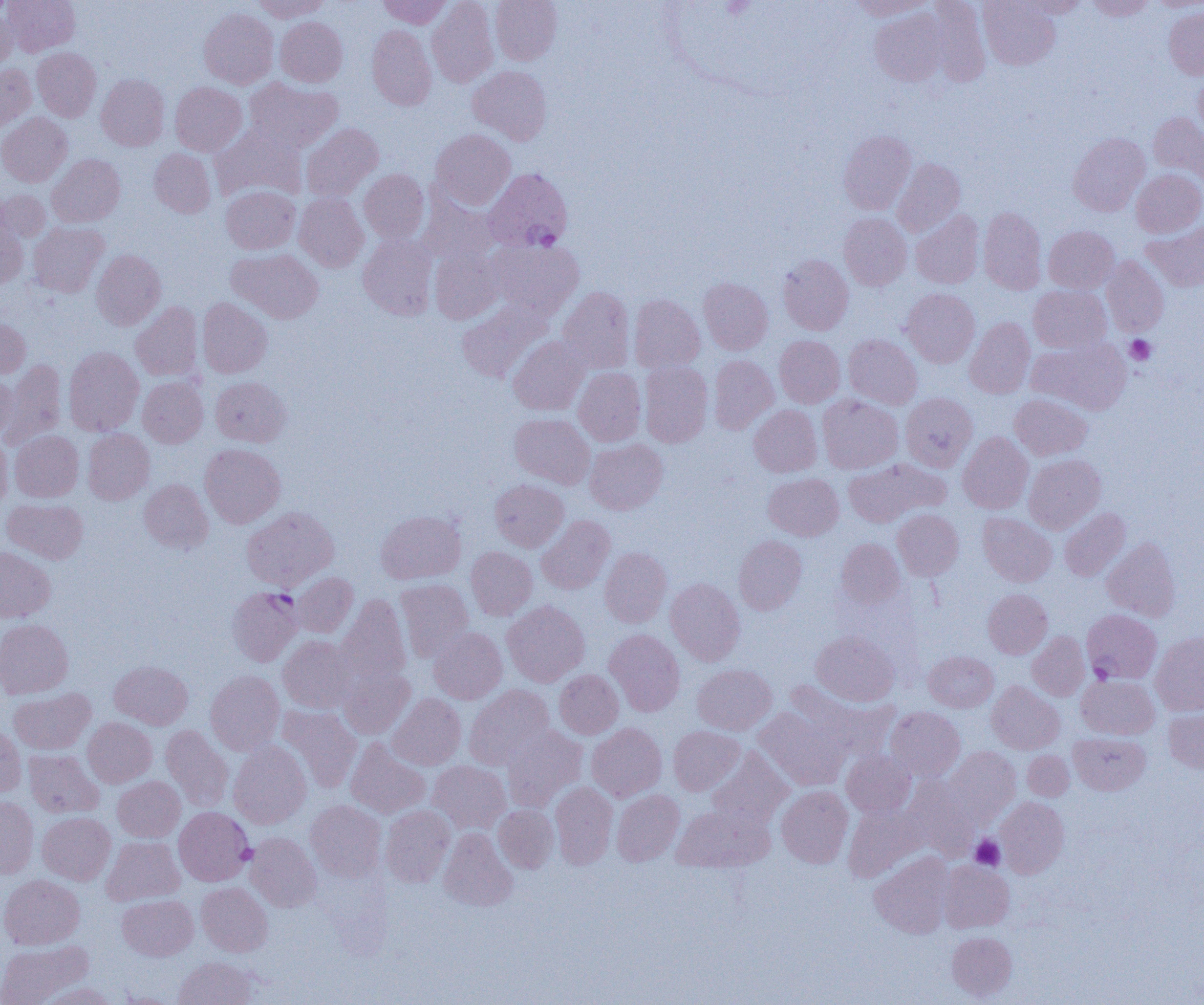

Approximate bounding boxes as [x1, y1, x2, y2] in pixels. Plasmodium falciparum-infected red blood cell locations: [484, 167, 573, 253], [228, 588, 304, 668], [1082, 609, 1161, 684]. Platelet locations: [1125, 335, 1156, 365], [970, 834, 1005, 870], [236, 844, 257, 865]. Uninfected red blood cell locations: [4, 0, 79, 56], [252, 0, 331, 21], [378, 0, 451, 28], [427, 0, 498, 87], [491, 0, 562, 65], [849, 0, 934, 20], [925, 0, 991, 86], [978, 0, 1060, 69], [1016, 0, 1088, 18], [1085, 0, 1155, 20], [1151, 1, 1204, 11], [1164, 7, 1204, 79], [0, 8, 17, 71], [199, 8, 278, 89], [871, 8, 948, 86], [275, 17, 348, 87], [367, 25, 436, 110], [32, 47, 100, 121], [0, 64, 36, 132], [468, 66, 552, 144], [1194, 71, 1204, 139], [96, 74, 169, 151], [244, 77, 343, 153], [170, 82, 247, 156], [1148, 112, 1204, 185], [0, 113, 72, 187], [211, 124, 306, 202], [301, 124, 383, 201], [431, 129, 515, 210], [838, 130, 916, 214], [1067, 132, 1149, 216], [149, 149, 215, 217], [47, 154, 125, 227], [893, 158, 965, 237], [359, 169, 429, 244], [1131, 169, 1204, 237], [221, 186, 300, 254], [0, 189, 50, 242], [294, 192, 368, 272], [419, 192, 498, 266], [978, 207, 1046, 294], [911, 210, 984, 288], [839, 213, 912, 290], [0, 217, 27, 289], [1141, 221, 1204, 292], [28, 222, 109, 297], [1044, 226, 1118, 293], [359, 234, 437, 320], [489, 238, 583, 318], [429, 247, 504, 324], [227, 248, 323, 323], [91, 249, 166, 330], [778, 254, 854, 335], [1101, 256, 1169, 336], [699, 277, 773, 354], [1028, 285, 1111, 353], [557, 286, 635, 374], [901, 288, 980, 367], [629, 294, 705, 372], [197, 298, 272, 377], [456, 300, 552, 383], [131, 302, 203, 381], [0, 317, 31, 378], [965, 317, 1035, 398], [843, 334, 921, 409], [775, 335, 845, 408], [508, 336, 589, 415], [1027, 338, 1132, 415], [63, 346, 144, 436], [708, 355, 778, 434], [2, 360, 67, 448], [639, 362, 713, 447], [573, 367, 646, 446], [0, 373, 17, 441], [138, 376, 208, 447], [211, 377, 291, 447], [901, 392, 978, 472], [817, 394, 903, 474], [1010, 394, 1092, 460], [749, 405, 822, 477], [509, 413, 595, 488], [83, 429, 154, 504], [10, 430, 83, 502], [958, 431, 1033, 513], [0, 432, 12, 512], [585, 439, 667, 514], [200, 443, 285, 528], [1024, 454, 1105, 534], [844, 458, 949, 527], [763, 473, 843, 541], [139, 479, 213, 553], [490, 479, 568, 551], [2, 498, 87, 564], [241, 507, 338, 591], [1059, 507, 1130, 581], [892, 509, 963, 580], [375, 510, 465, 584], [978, 512, 1056, 586], [537, 515, 615, 594], [734, 535, 807, 615], [1102, 537, 1180, 621], [836, 538, 905, 608], [0, 546, 55, 622], [466, 546, 537, 620], [600, 547, 672, 627], [291, 572, 358, 638], [665, 578, 745, 666], [395, 579, 474, 662], [983, 588, 1052, 658], [337, 594, 411, 686], [503, 601, 589, 686], [0, 619, 73, 699], [429, 627, 507, 704], [604, 629, 685, 716], [811, 630, 899, 706], [1027, 631, 1090, 700], [1151, 633, 1204, 715], [278, 636, 359, 713], [924, 651, 998, 712], [110, 661, 192, 729], [692, 664, 776, 734], [338, 667, 415, 739], [554, 669, 623, 739], [205, 670, 285, 755], [1076, 675, 1159, 738], [987, 681, 1064, 754], [464, 685, 554, 769], [9, 688, 95, 755], [388, 694, 466, 770], [276, 705, 362, 793], [754, 707, 848, 791], [886, 707, 965, 781], [1164, 708, 1204, 773], [83, 717, 156, 787], [0, 723, 26, 797], [586, 723, 666, 801], [161, 725, 234, 812], [501, 725, 587, 812], [668, 726, 744, 795], [1069, 732, 1150, 795], [346, 738, 431, 819], [229, 741, 311, 828], [944, 747, 1020, 826], [708, 748, 793, 828], [24, 749, 103, 818], [841, 750, 915, 817], [1022, 751, 1073, 800], [428, 761, 511, 834], [113, 776, 185, 842], [902, 780, 979, 860], [550, 781, 618, 869], [777, 786, 853, 867], [612, 790, 684, 865], [0, 797, 39, 878], [995, 797, 1069, 878], [305, 800, 386, 882], [672, 803, 774, 872], [493, 804, 559, 872], [380, 805, 455, 887], [844, 805, 924, 882], [174, 807, 254, 885], [37, 812, 114, 884], [438, 828, 517, 911], [245, 832, 321, 912], [102, 836, 184, 905], [870, 852, 954, 938], [939, 861, 1014, 932], [0, 874, 85, 949], [196, 882, 272, 956], [117, 895, 198, 960], [946, 932, 1017, 1000], [0, 940, 92, 1004], [173, 956, 258, 1004], [37, 983, 118, 1005]. Slide-level diagnosis: Plasmodium falciparum. Thin blood film. One field of a larger specimen. Image is 1204×1005 pixels. 1000x magnification. Optical microscopy.